Identify the blood parasite species.
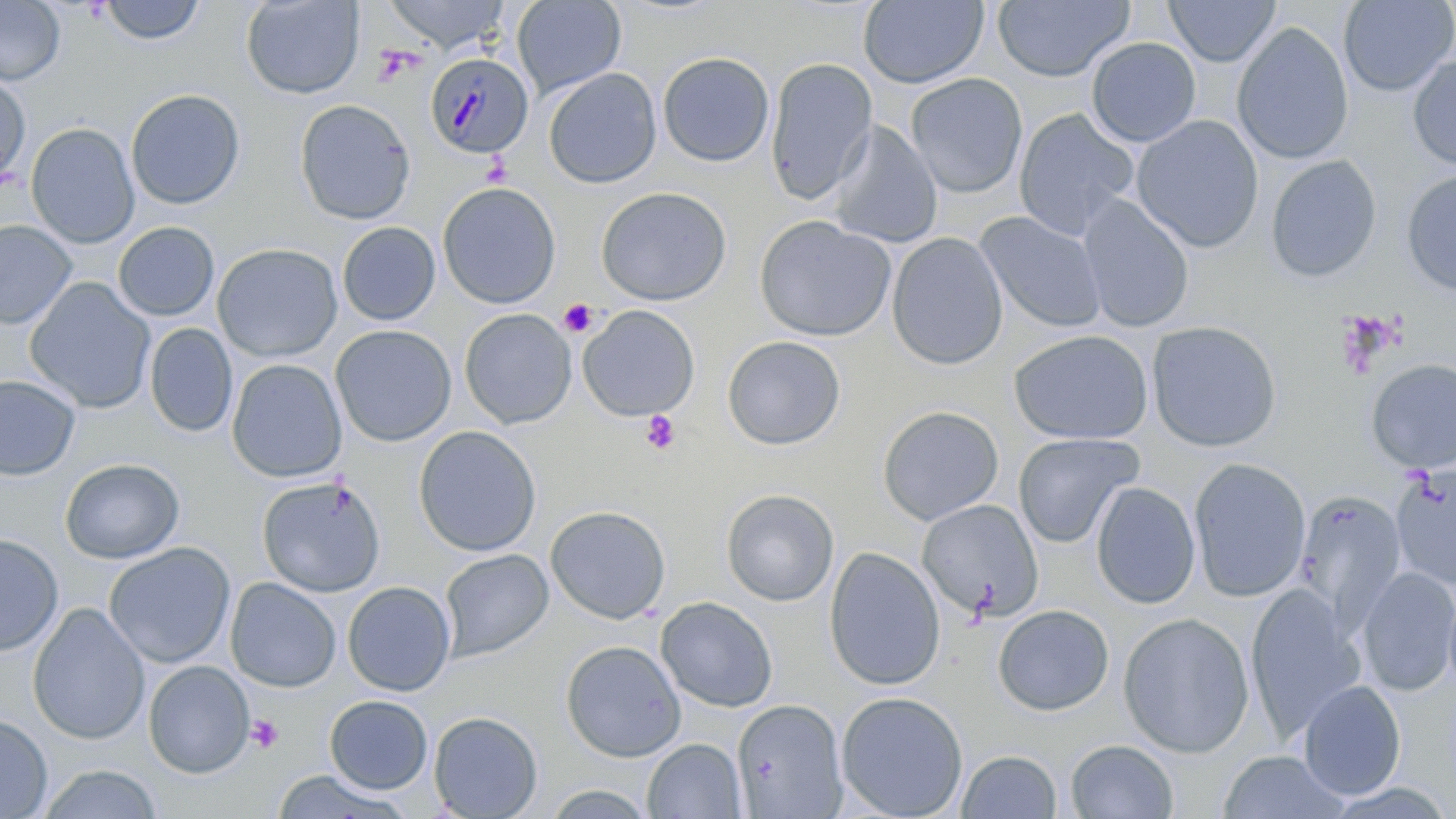
Plasmodium malariae.

Approximate bounding boxes as (x1,y1)-(x2,y2) corner pairs in pixels. Plasmodium malariae-infected red blood cell locations: (424,52)-(534,159). Platelet locations: (558,298)-(598,337), (640,410)-(680,455), (246,714)-(284,754). Uninfected red blood cell locations: (0,0)-(65,86), (382,0)-(512,55), (511,0)-(626,98), (858,0)-(989,89), (1164,0)-(1281,67), (1338,0)-(1455,97), (97,1)-(207,45), (240,1)-(365,99), (992,1)-(1133,82), (1231,21)-(1354,165), (1086,37)-(1201,147), (657,52)-(774,167), (1408,54)-(1456,172), (764,57)-(878,205), (543,67)-(662,188), (0,73)-(31,189), (906,73)-(1028,198), (126,89)-(246,209), (295,98)-(415,225), (1013,107)-(1139,239), (1131,114)-(1264,253), (828,121)-(943,248), (25,122)-(140,248), (1265,155)-(1382,283), (1401,169)-(1456,296), (437,182)-(561,309), (596,186)-(732,306), (1078,193)-(1195,333), (975,211)-(1108,333), (754,215)-(895,342), (0,219)-(77,329), (113,221)-(219,321), (337,222)-(441,326), (886,232)-(1007,370), (212,243)-(343,362), (24,277)-(156,414), (577,305)-(700,422), (459,308)-(577,429), (1146,320)-(1283,452), (144,323)-(238,438), (331,324)-(456,447), (1009,329)-(1154,445), (722,336)-(846,451), (227,358)-(347,483), (1366,359)-(1456,473), (0,374)-(81,481), (877,405)-(1004,525), (413,425)-(541,557), (1013,432)-(1143,549), (60,458)-(184,564), (1189,458)-(1311,602), (1392,465)-(1456,591), (256,476)-(386,597), (1091,481)-(1201,609), (720,488)-(839,606), (1295,492)-(1407,624), (917,498)-(1043,621), (545,505)-(671,624), (0,534)-(63,656), (103,542)-(236,668), (824,546)-(946,691), (438,549)-(553,661), (1356,567)-(1456,696), (226,577)-(341,692), (342,581)-(455,696), (1443,584)-(1456,701), (1245,586)-(1364,742), (655,597)-(778,712), (28,603)-(150,746), (993,604)-(1114,716), (1117,612)-(1255,758), (560,640)-(686,761), (143,660)-(255,778), (1298,680)-(1406,800), (836,691)-(968,819), (325,695)-(433,794), (732,699)-(849,818), (428,711)-(543,819), (0,715)-(52,818), (643,738)-(746,819), (1066,739)-(1178,818), (956,749)-(1062,818), (1217,750)-(1350,819), (36,764)-(164,819), (270,769)-(414,818), (542,784)-(656,819). May-Grünwald-Giemsa stain. Light microscopy. Captured at 1000x magnification. Thin blood film. Image is 1456×819 pixels. One field of a larger specimen.